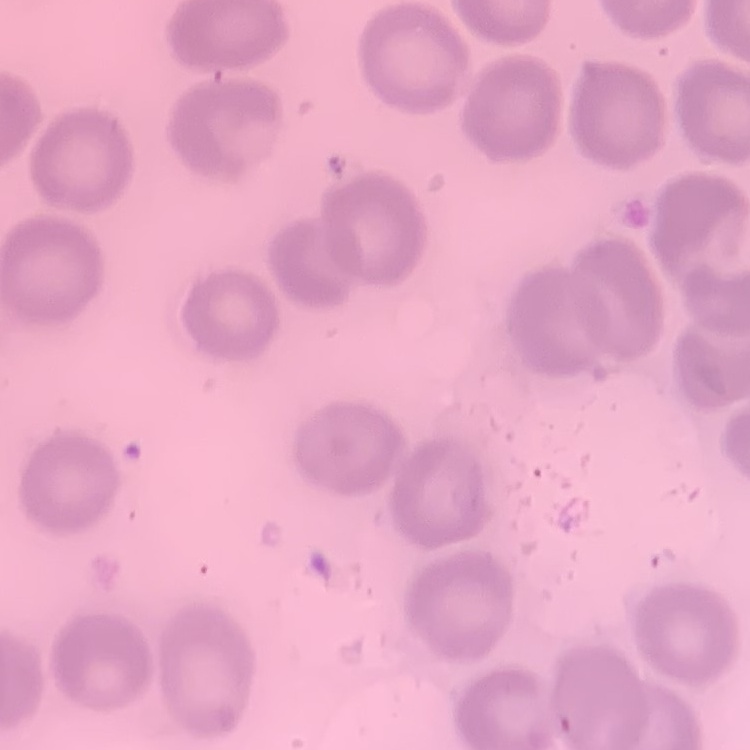

erythrocyte morphology = no rouleaux formation
image type = one tile cut from a larger photomicrograph
preparation = thin blood film
stain = Field's or Giemsa